State which parasite is depicted.
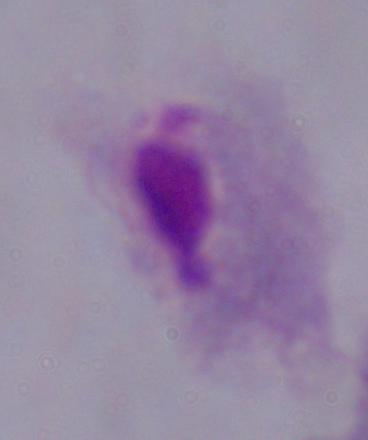

This is a trichomonad.

Summary:
  - Magnification: 1000x
  - Modality: micrograph